Classify this cell by malaria status.
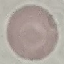
Uninfected.

image type = automatically extracted cell patch, resized to 64 × 64 pixels
capture = smartphone through the microscope eyepiece
preparation = thin blood film
stain = Giemsa